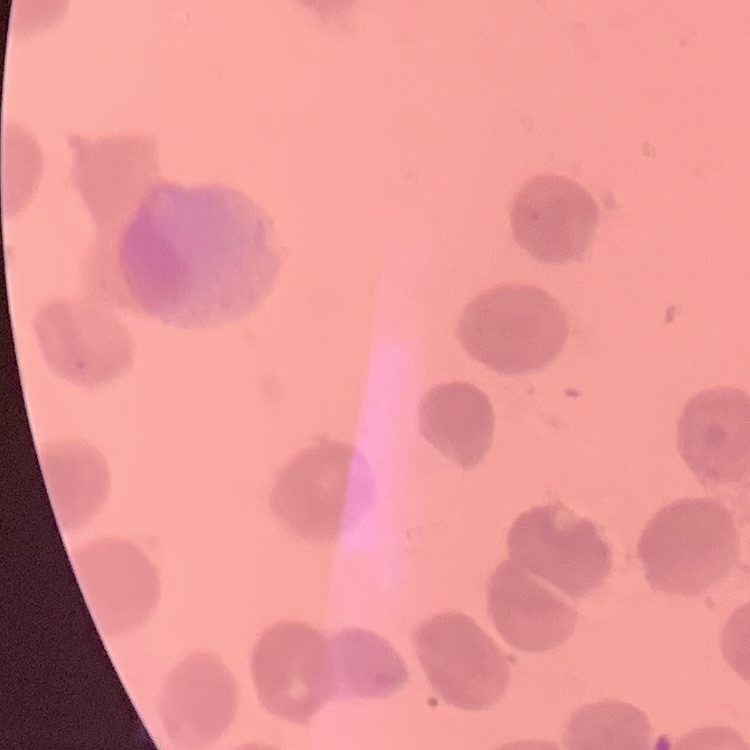

red blood cell morphology = no rouleaux formation
stain = Field's or Giemsa
image type = square crop of a larger photomicrograph
preparation = thin peripheral smear